Name the parasite shown.
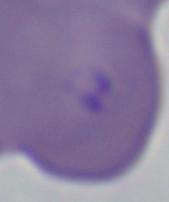
Babesia.

magnification = 1000x
modality = micrograph